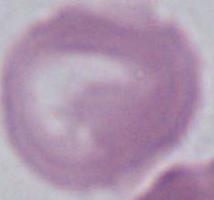 A red blood cell is seen. Captured at 1000x magnification. Micrograph.